State which parasite is depicted.
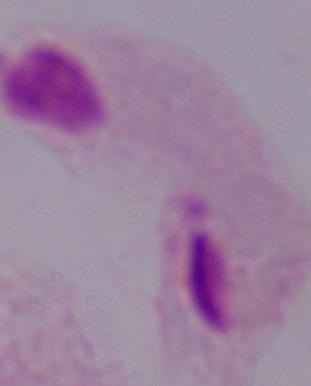
A trichomonad.

1000x magnification. Photomicrograph.